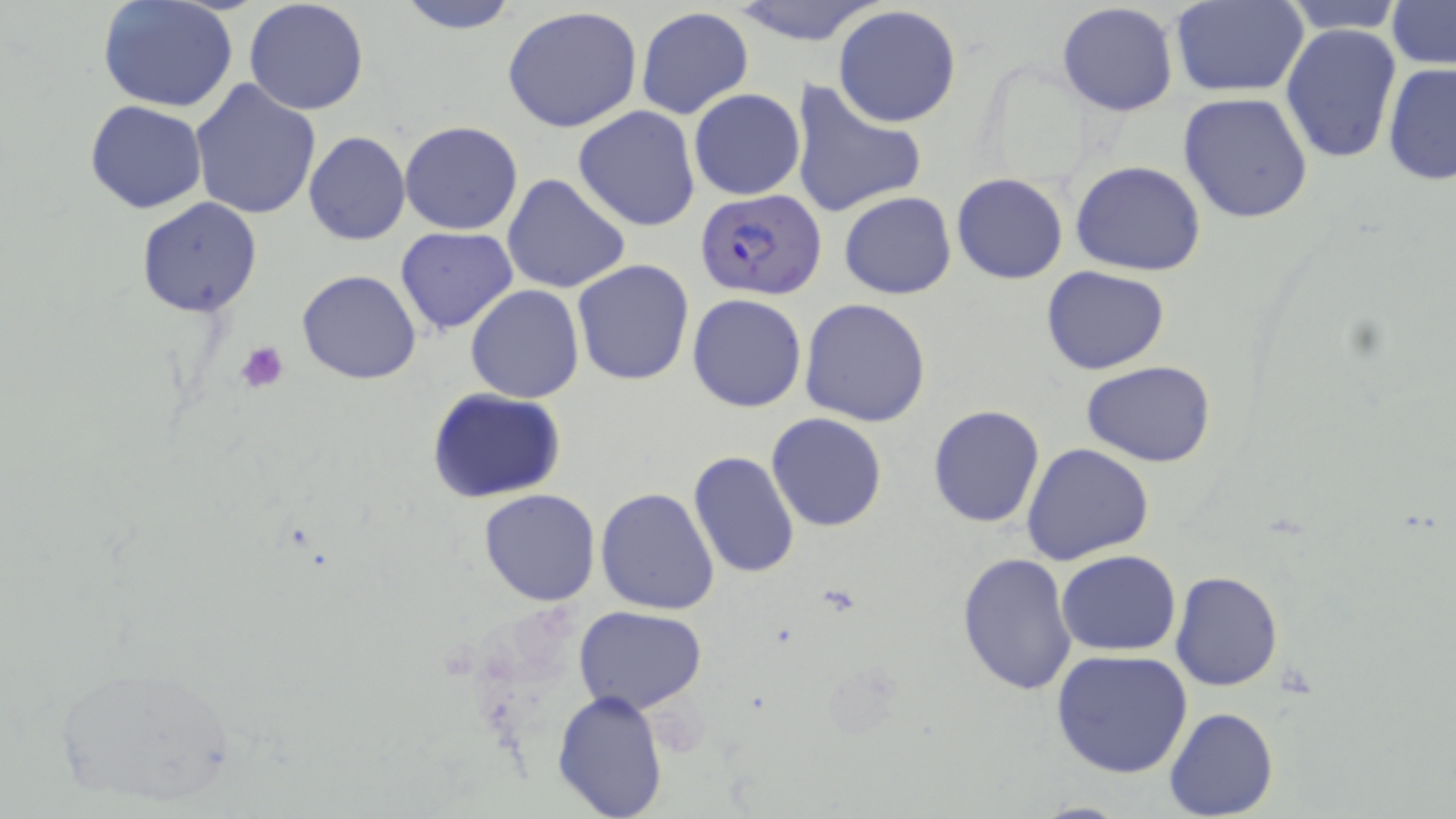
Approximate bounding boxes as (x1, y1, x2, y2) in pixels. Platelet locations: (233, 340, 289, 395). Plasmodium falciparum-infected red blood cell locations: (694, 187, 828, 301). Uninfected red blood cell locations: (393, 0, 521, 34), (721, 0, 886, 47), (1281, 0, 1405, 33), (1386, 0, 1456, 69), (243, 1, 370, 116), (1169, 1, 1310, 97), (97, 2, 241, 112), (1057, 3, 1179, 116), (832, 5, 962, 128), (502, 6, 644, 132), (636, 8, 753, 120), (1280, 23, 1401, 165), (1382, 62, 1456, 186), (189, 78, 323, 218), (792, 81, 925, 219), (689, 88, 805, 200), (1176, 92, 1315, 225), (83, 99, 207, 213), (574, 106, 700, 232), (400, 120, 524, 235), (303, 130, 411, 246), (1069, 159, 1208, 276), (950, 173, 1068, 284), (502, 174, 630, 294), (839, 192, 956, 300), (137, 197, 264, 318), (395, 227, 519, 335), (573, 260, 693, 386), (1042, 266, 1170, 375), (298, 269, 420, 385), (466, 284, 583, 402), (687, 293, 807, 413), (799, 298, 932, 427), (1082, 359, 1216, 467), (426, 387, 568, 503), (927, 404, 1046, 528), (766, 412, 888, 532), (1022, 443, 1155, 566), (688, 453, 800, 579), (596, 487, 720, 616), (478, 488, 600, 606), (1057, 549, 1181, 656), (955, 552, 1077, 696), (1170, 571, 1283, 693), (575, 605, 706, 714), (1050, 649, 1194, 777), (48, 660, 240, 810), (553, 688, 669, 817), (1164, 707, 1279, 819), (1027, 800, 1138, 817). Slide-level diagnosis: Plasmodium falciparum. May-Grünwald-Giemsa-stained preparation. One field of a larger specimen. Light microscopy. Image is 1456×819 pixels. 1000x magnification. Thin blood smear.